Assess this cell for malaria.
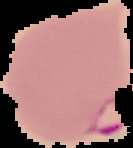
It is parasitized.

Summary:
  - Image type: segmented cell region with the area outside set to black
  - Image size: 133×148 pixels
  - Preparation: thin blood film